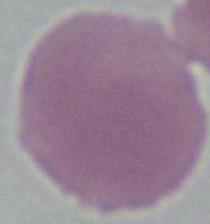
Captured at 1000x magnification. An erythrocyte is shown. Micrograph.